Assess this cell for malaria.
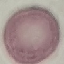
It is uninfected.

Cell patch, automatically extracted from a larger field of view and resized to 64 × 64 pixels. Giemsa-stained preparation. Photographed with a smartphone camera at the microscope eyepiece. Thin blood film.